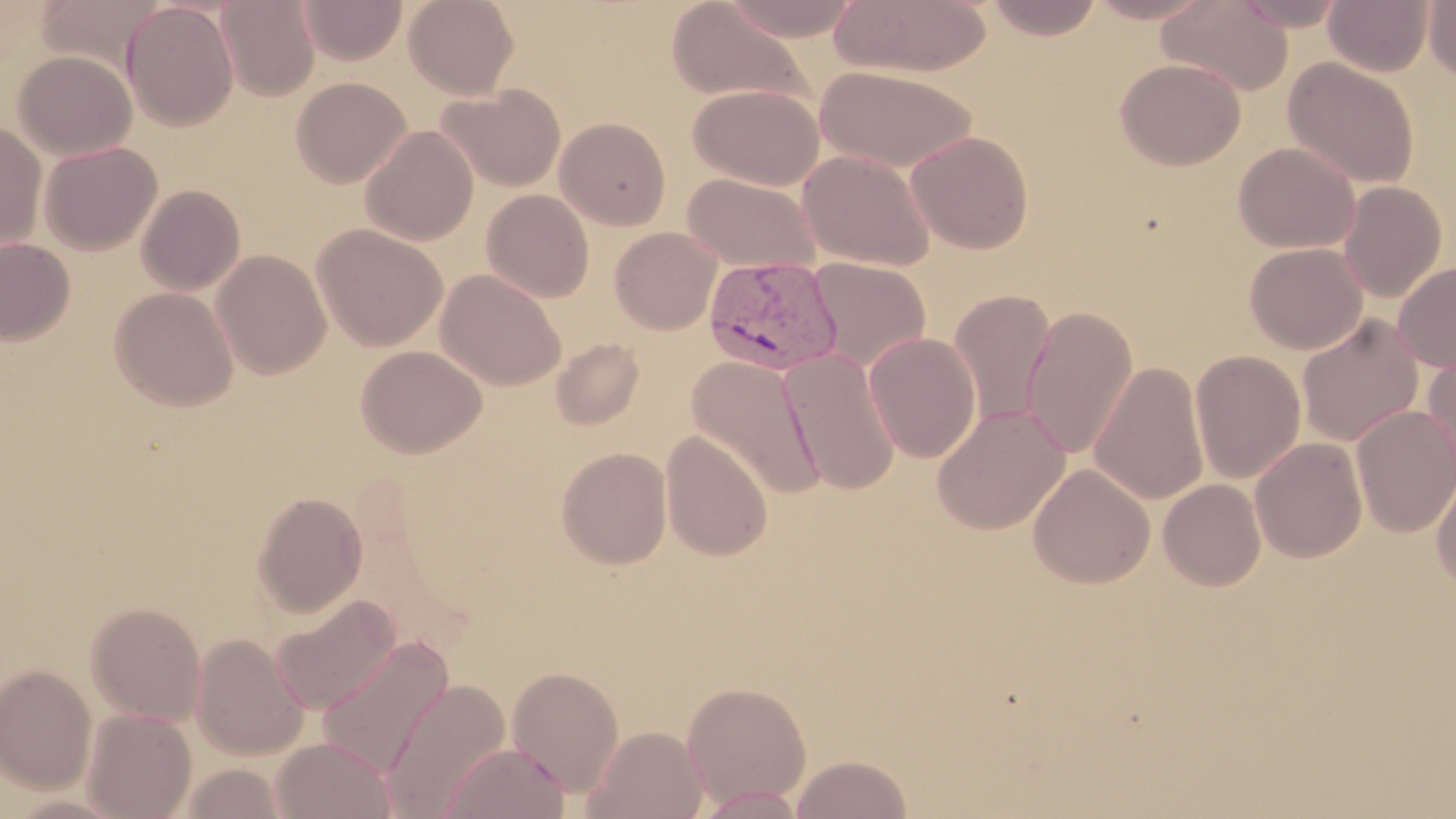

Summary:
  - Coordinate format: approximate bounding boxes as [x1, y1, x2, y2] in pixels
  - Plasmodium vivax-infected red blood cell locations: [704, 255, 845, 376]
  - Uninfected red blood cell locations: [403, 0, 520, 99], [719, 0, 863, 41], [830, 0, 991, 78], [983, 0, 1105, 40], [1084, 0, 1215, 24], [1157, 0, 1293, 96], [1231, 0, 1348, 31], [1323, 0, 1435, 76], [1424, 0, 1456, 84], [215, 1, 320, 101], [298, 1, 407, 65], [666, 1, 812, 106], [122, 2, 238, 130], [13, 50, 137, 160], [1282, 57, 1420, 190], [1115, 58, 1246, 170], [815, 65, 978, 172], [291, 76, 411, 188], [436, 84, 566, 192], [688, 84, 824, 190], [555, 117, 671, 230], [0, 121, 47, 253], [359, 124, 478, 245], [906, 131, 1034, 254], [39, 141, 162, 255], [1233, 142, 1360, 253], [797, 149, 937, 271], [684, 173, 822, 273], [1338, 181, 1447, 302], [137, 185, 245, 295], [481, 189, 594, 303], [313, 224, 447, 351], [610, 227, 722, 334], [0, 237, 75, 345], [1244, 242, 1367, 354], [212, 249, 331, 379], [807, 257, 930, 372], [1393, 261, 1456, 372], [436, 269, 565, 391], [109, 286, 238, 411], [948, 289, 1056, 427], [1022, 305, 1138, 459], [1296, 315, 1424, 447], [863, 332, 981, 462], [550, 337, 644, 430], [356, 344, 487, 459], [779, 349, 901, 496], [1190, 349, 1306, 484], [1422, 351, 1456, 486], [687, 355, 826, 501], [1089, 361, 1210, 506], [932, 404, 1070, 534], [1351, 405, 1456, 537], [661, 430, 773, 562], [1249, 437, 1367, 562], [555, 446, 673, 569], [1027, 462, 1155, 589], [1432, 471, 1456, 590], [1158, 478, 1267, 591], [251, 492, 368, 617], [270, 594, 400, 715], [85, 602, 206, 725], [190, 633, 308, 761], [316, 635, 454, 780], [0, 663, 97, 794], [506, 665, 626, 797], [380, 677, 512, 818], [681, 680, 812, 809], [82, 708, 197, 819], [585, 725, 708, 819], [271, 736, 398, 818], [440, 741, 571, 819], [790, 754, 912, 818], [179, 763, 288, 819], [695, 786, 808, 818], [4, 792, 134, 818]
  - Slide-level diagnosis: Plasmodium vivax
  - Field of view: single
  - Magnification: 1000x
  - Modality: optical microscopy
  - Image size: 1456×819 pixels
  - Preparation: thin blood film
  - Stain: May-Grünwald-Giemsa